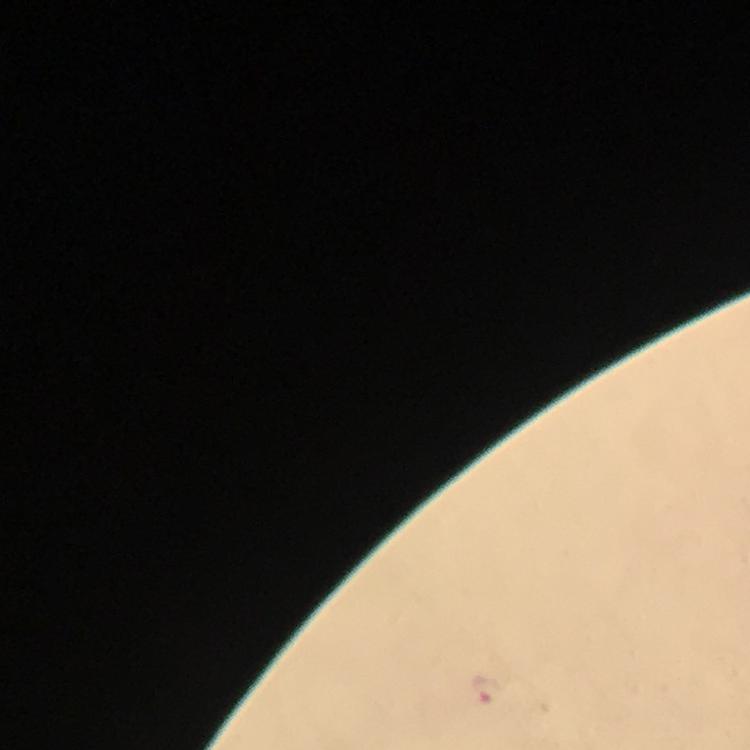 Approximate centers as [x, y] in pixels. Malaria parasite locations: [487, 692]. A crop from one field of view. Image is 750×750 pixels. Thick blood film. Immersion oil applied. At 100x magnification. Giemsa-stained preparation. From a malaria diagnostic workup. Photographed through the microscope with a smartphone camera.